Report the malaria status of this cell.
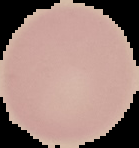
Uninfected.

image_size: 139×148 pixels
image_type: segmented cell region with the area outside set to black
preparation: thin blood film